Point out each leukocyte.
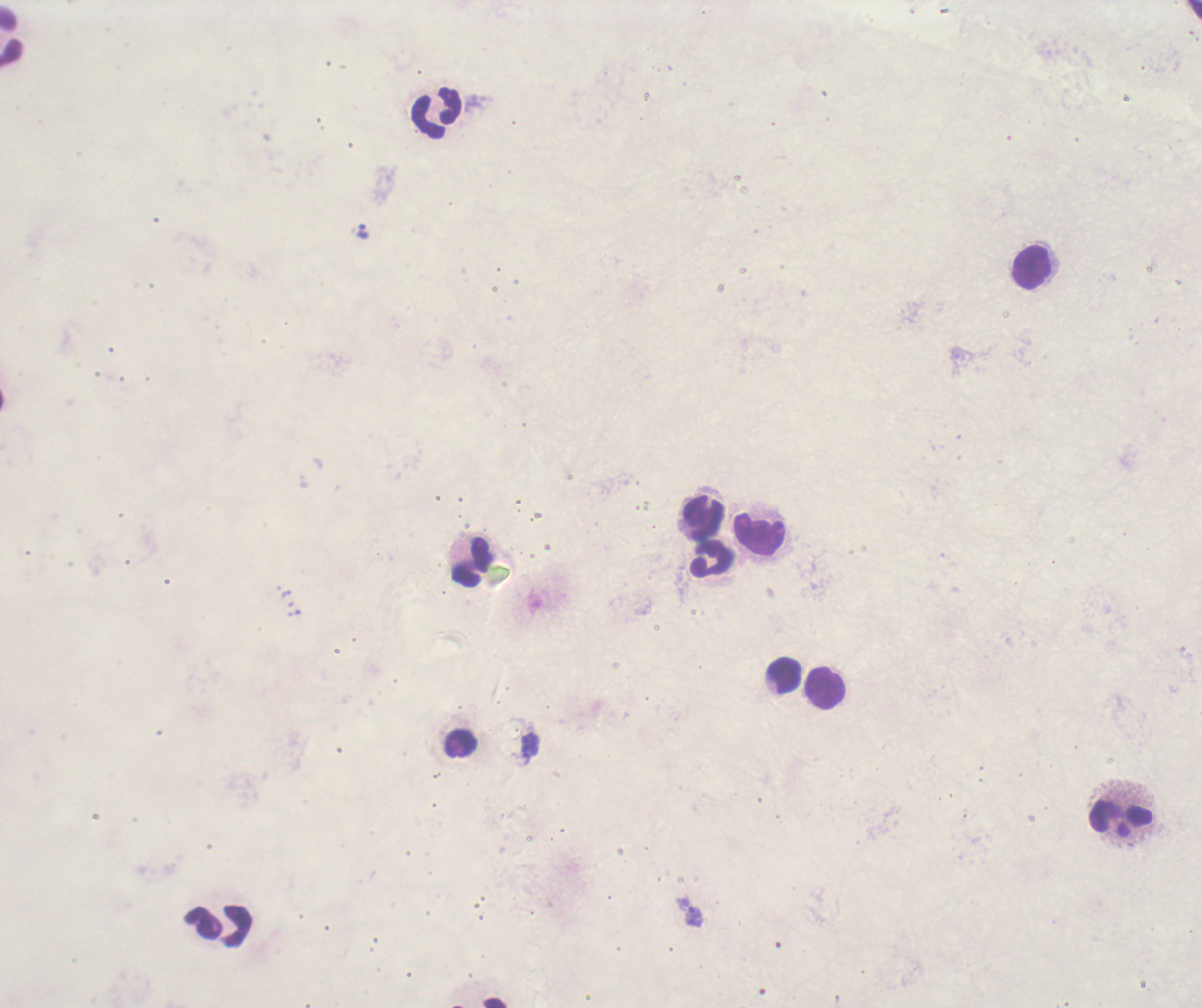

Approximate centers as (x, y) in pixels.
Leukocytes: (11, 36), (437, 112), (1033, 267), (704, 518), (758, 532), (711, 561), (472, 562), (785, 675), (824, 688), (461, 742), (1121, 819), (218, 925).

Approximate centers as (x, y) in pixels.
Summary:
  - Trophozoite locations: (362, 230), (530, 741), (526, 760), (693, 916)
  - Result: positive for malaria parasites
  - Image size: 1202×1008 pixels
  - Field of view: single
  - Preparation: thick blood film
  - Background quality: poor
  - Stain: Romanowsky
  - Coloration quality: bad
  - Magnification: 100x
  - Context: previously used in an actual diagnosis